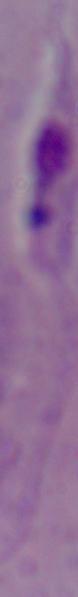

Summary:
  - Modality: photomicrograph
  - Identification: Leishmania
  - Magnification: 1000x